Name the parasite shown.
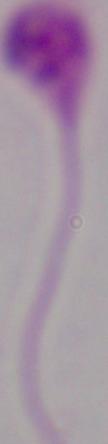
This is Leishmania.

Summary:
  - Magnification: 1000x
  - Modality: photomicrograph